Report the malaria status of this cell.
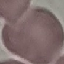
Uninfected.

Summary:
  - Preparation: thin smear
  - Stain: Giemsa
  - Image type: cell patch, automatically extracted from a larger field of view and resized to 64 × 64 pixels
  - Capture: smartphone camera at the microscope eyepiece